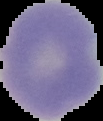
malaria status = uninfected
preparation = thin blood smear
image type = segmented cell region with the area outside set to black
image size = 103×121 pixels